Name the parasite shown.
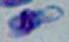
Toxoplasma gondii.

Summary:
  - Magnification: 1000x
  - Modality: photomicrograph